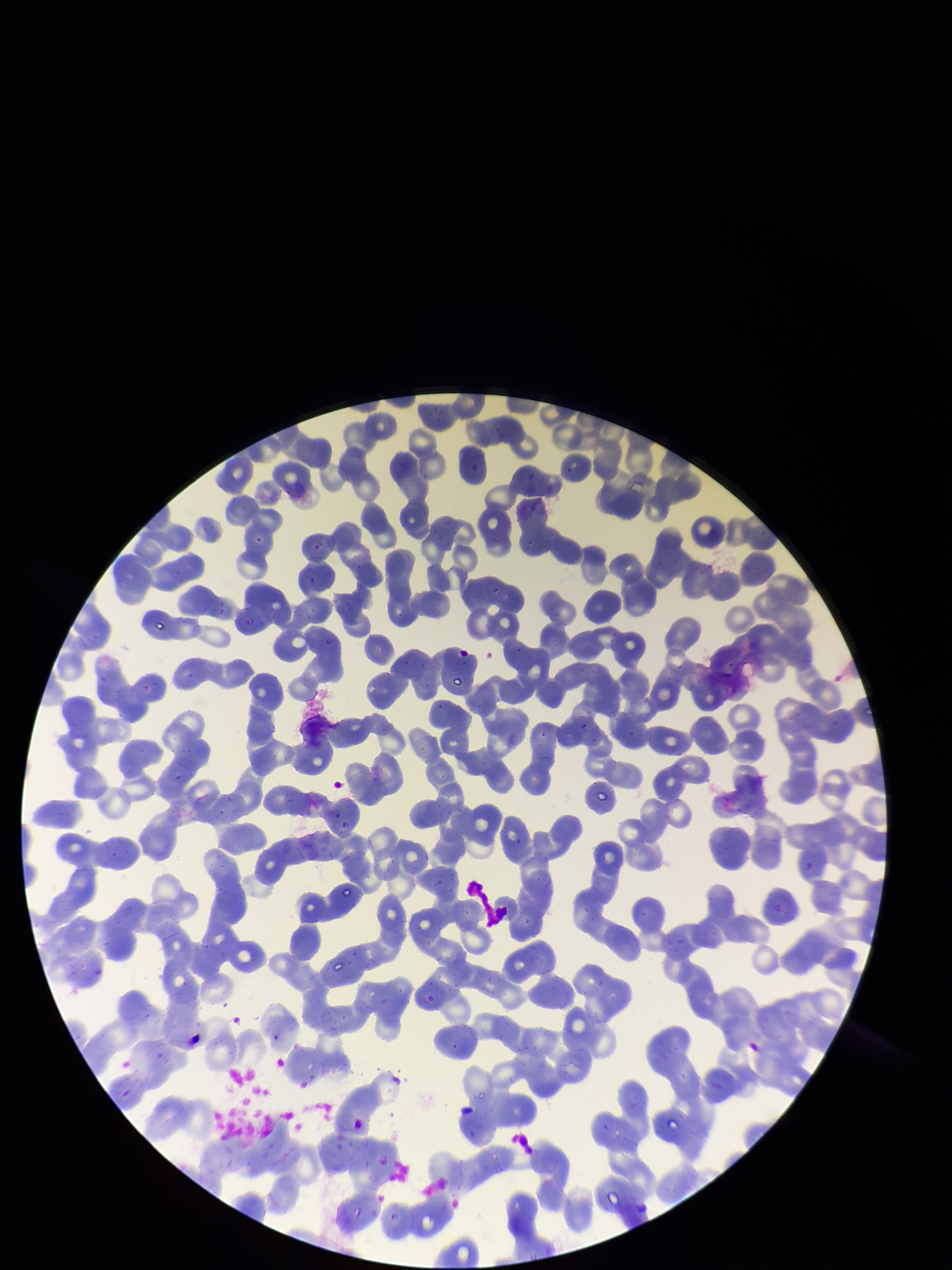 Red blood cell count: 264. Parasitized red blood cell count: 0. Preparation: thin blood smear. Single field of view. Smartphone photograph taken through the eyepiece of a microscope. Stained with Giemsa. Image is 952×1270 pixels. Patient malaria status: negative. Parasitized red blood cells: none identified.